Locate every blood parasite and identify its species.
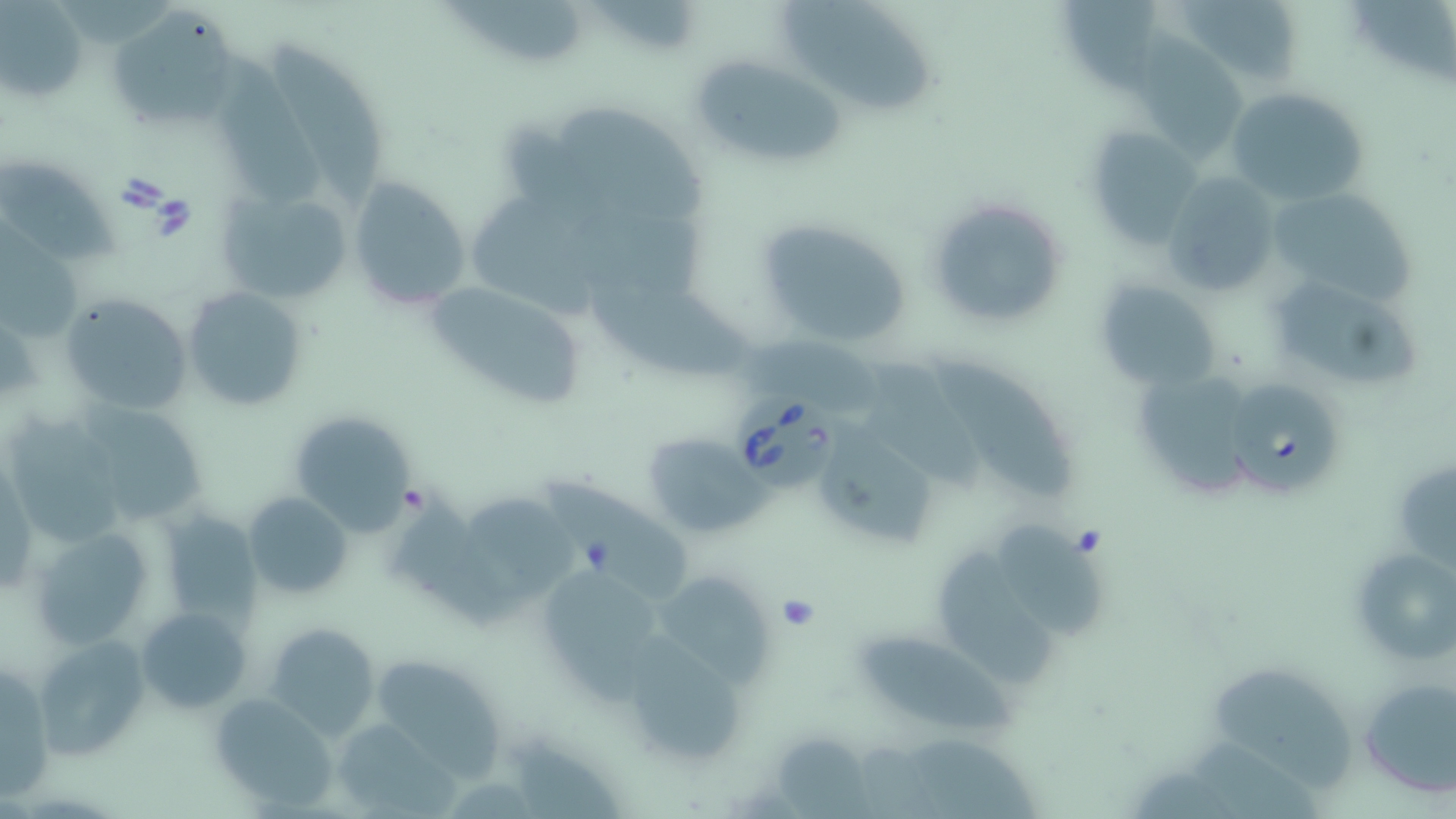

Approximate bounding boxes as (x1, y1, x2, y2) in pixels.
Babesia divergens-infected red blood cells: (1228, 381, 1342, 491), (726, 385, 848, 497).
No Plasmodium falciparum, Plasmodium ovale, Plasmodium malariae, Plasmodium vivax, or Trypanosoma brucei observed.

{
  "slide_level_diagnosis": "Babesia divergens",
  "image_size": "1456×819 pixels",
  "preparation": "thin blood film",
  "modality": "optical microscopy",
  "uninfected_red_blood_cell_locations": "approximate bounding boxes as (x1, y1, x2, y2) in pixels: (445, 0, 590, 65), (780, 0, 933, 116), (1179, 1, 1308, 88), (2, 2, 87, 104), (1067, 3, 1162, 107), (106, 9, 238, 131), (273, 42, 384, 204), (220, 43, 316, 203), (1132, 43, 1246, 158), (691, 54, 841, 161), (1225, 87, 1368, 205), (560, 102, 706, 221), (1085, 126, 1203, 247), (0, 152, 119, 271), (1162, 172, 1282, 299), (349, 176, 471, 310), (1262, 186, 1417, 308), (214, 187, 353, 307), (469, 194, 622, 324), (925, 195, 1070, 330), (0, 216, 87, 342), (750, 217, 914, 350), (582, 273, 751, 379), (1274, 276, 1419, 385), (1095, 279, 1223, 394), (425, 280, 583, 409), (182, 286, 307, 412), (60, 292, 193, 417), (859, 358, 981, 491), (935, 358, 1082, 508), (1139, 373, 1253, 501), (85, 398, 204, 520), (287, 410, 416, 536), (827, 422, 941, 546), (642, 432, 761, 537), (548, 475, 692, 600), (397, 489, 524, 630), (243, 490, 354, 598), (467, 491, 574, 595), (159, 509, 261, 624), (1006, 520, 1108, 643), (30, 524, 159, 651), (1348, 542, 1454, 670), (943, 552, 1056, 691), (540, 566, 663, 709), (655, 571, 774, 689), (138, 606, 251, 712), (261, 621, 379, 739), (626, 628, 744, 758), (867, 630, 1032, 737), (33, 632, 150, 760), (1, 659, 53, 801), (381, 659, 506, 781), (1210, 667, 1356, 795), (1355, 674, 1455, 799), (209, 693, 337, 810), (327, 718, 454, 814)",
  "stain": "May-Grünwald-Giemsa",
  "field_of_view": "one of a larger specimen",
  "magnification": "1000x"
}